Assess this cell for malaria.
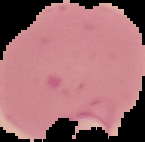
It is parasitized.

Image is 145×142 pixels. Cell region segmented out of the field of view; the surrounding area is masked to black. From a thin blood film.